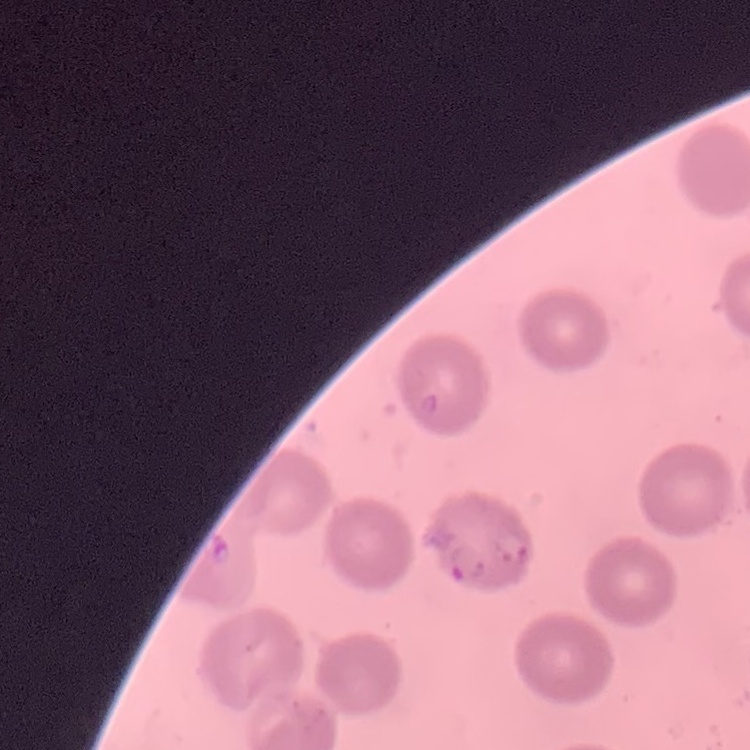

Summary:
  - Erythrocyte morphology: no rouleaux formation
  - Preparation: thin blood film
  - Stain: Field's or Giemsa
  - Image type: one tile cut from a larger photomicrograph